Report the malaria status of this cell.
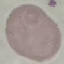

It is uninfected.

stain: Giemsa
capture: smartphone through the microscope eyepiece
preparation: thin blood film
image_type: cell patch, automatically extracted from a larger field of view and resized to 64 × 64 pixels